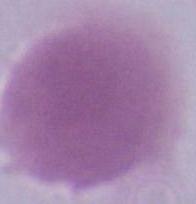
Summary:
  - Modality: micrograph
  - Identification: red blood cell
  - Magnification: 1000x